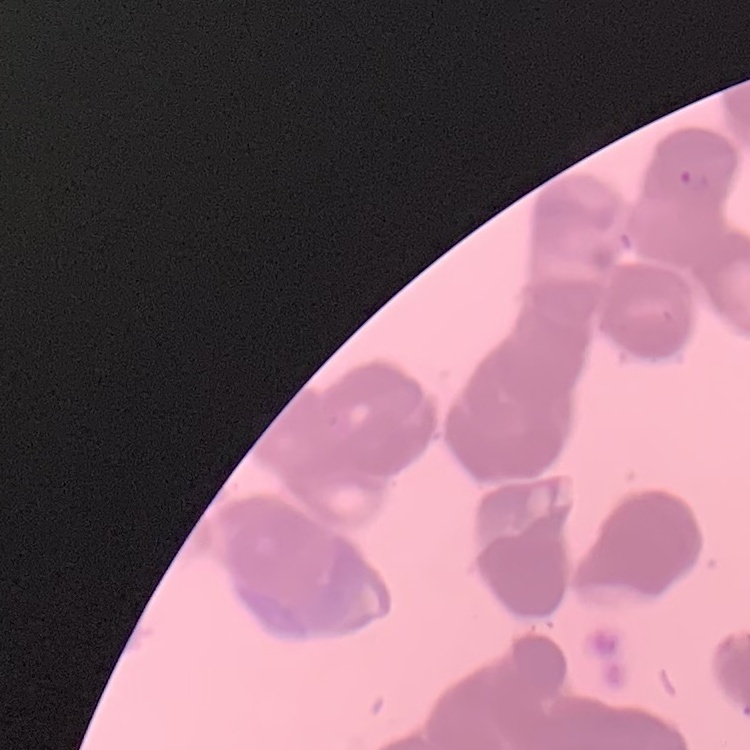

red blood cell morphology = rouleaux formation
preparation = thin blood film
image type = square crop of a larger photomicrograph
stain = Field's or Giemsa